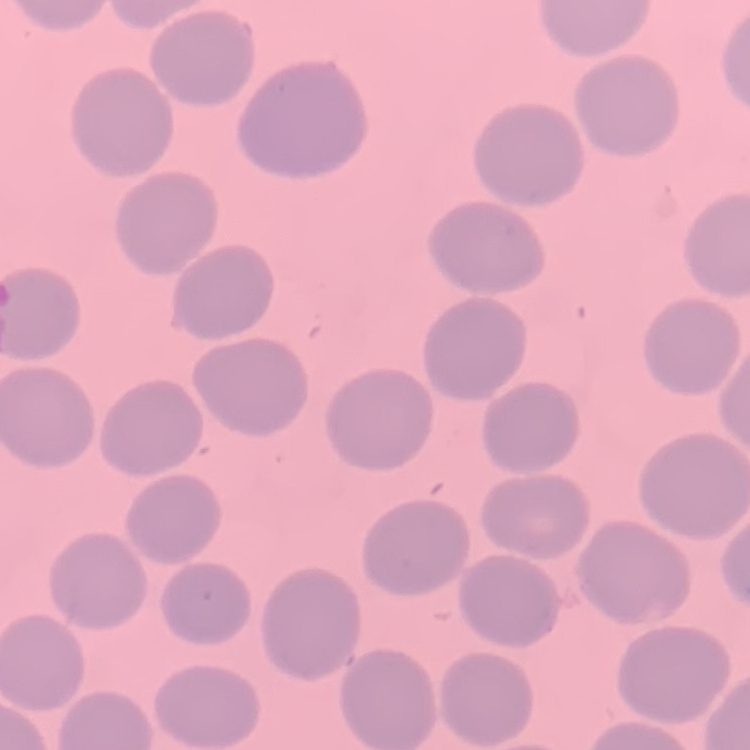
The red blood cells exhibit no rouleaux formation. Thin peripheral smear. Stained with either Field's or Giemsa. One tile cut from a larger photomicrograph.